Evaluate for parasitized red blood cells.
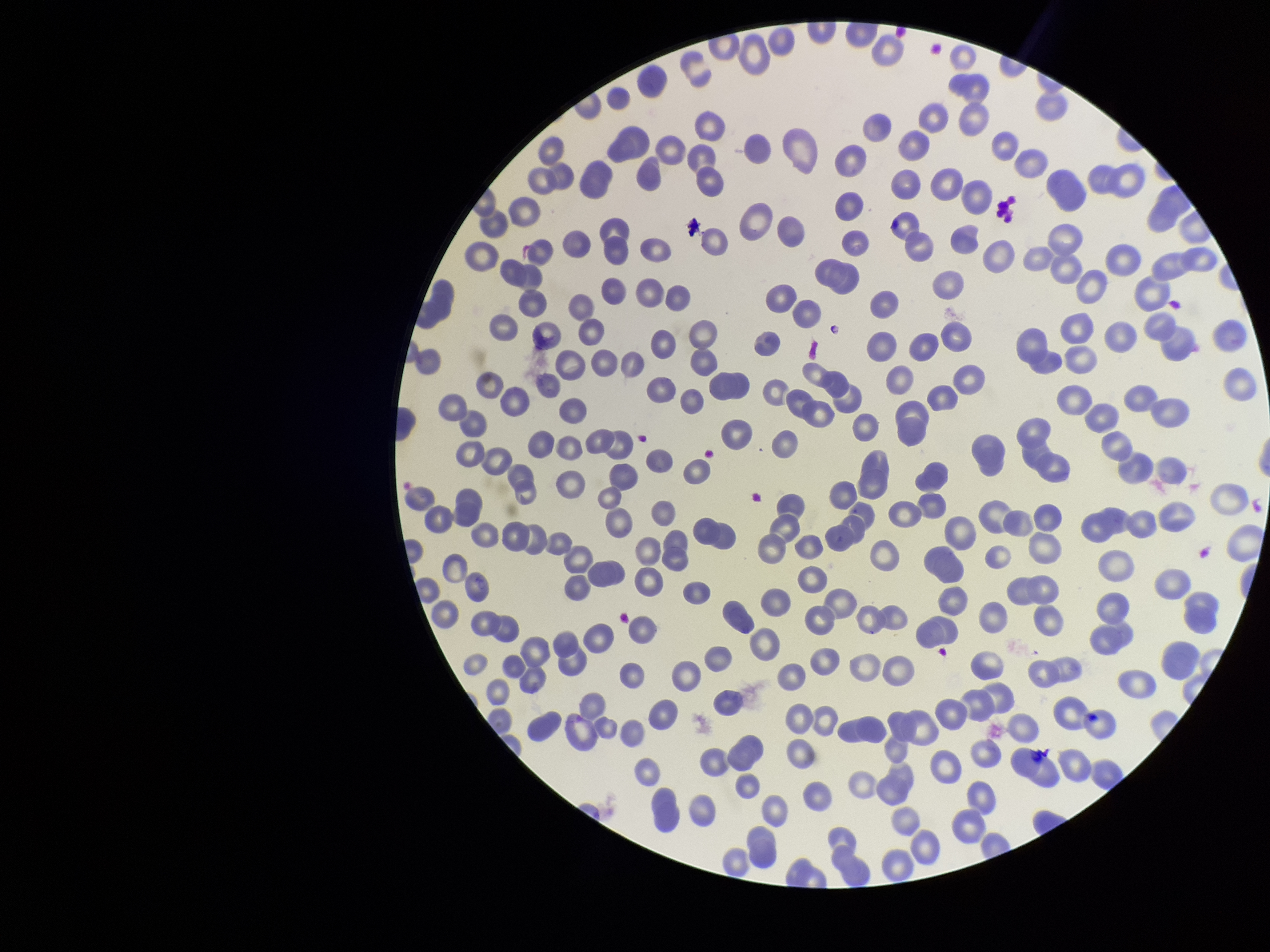
None seen.

Image is 1270×952 pixels. Stained with Giemsa. Photographed through the microscope eyepiece with a smartphone camera. Species reported for this patient: Plasmodium vivax. Parasitized red blood cell count: 0. Preparation: thin. Patient malaria status: positive. One field from this slide. Red blood cell count: 239.